Assess this cell for malaria.
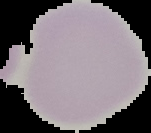

It is uninfected.

Image is 151×133 pixels. From a thin blood film. The area outside the segmented cell region is set to black.